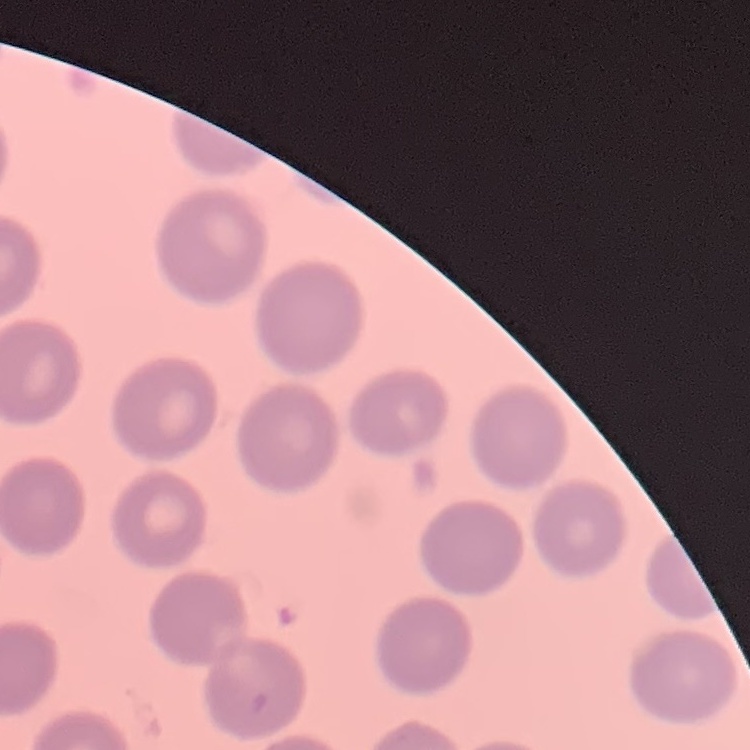

erythrocyte morphology = no rouleaux formation
image type = square crop of a larger photomicrograph
preparation = thin blood smear
stain = Field's or Giemsa